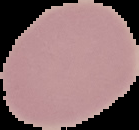
Summary:
  - Image size: 139×130 pixels
  - Preparation: thin blood film
  - Image type: segmented cell region on a black background
  - Malaria status: uninfected